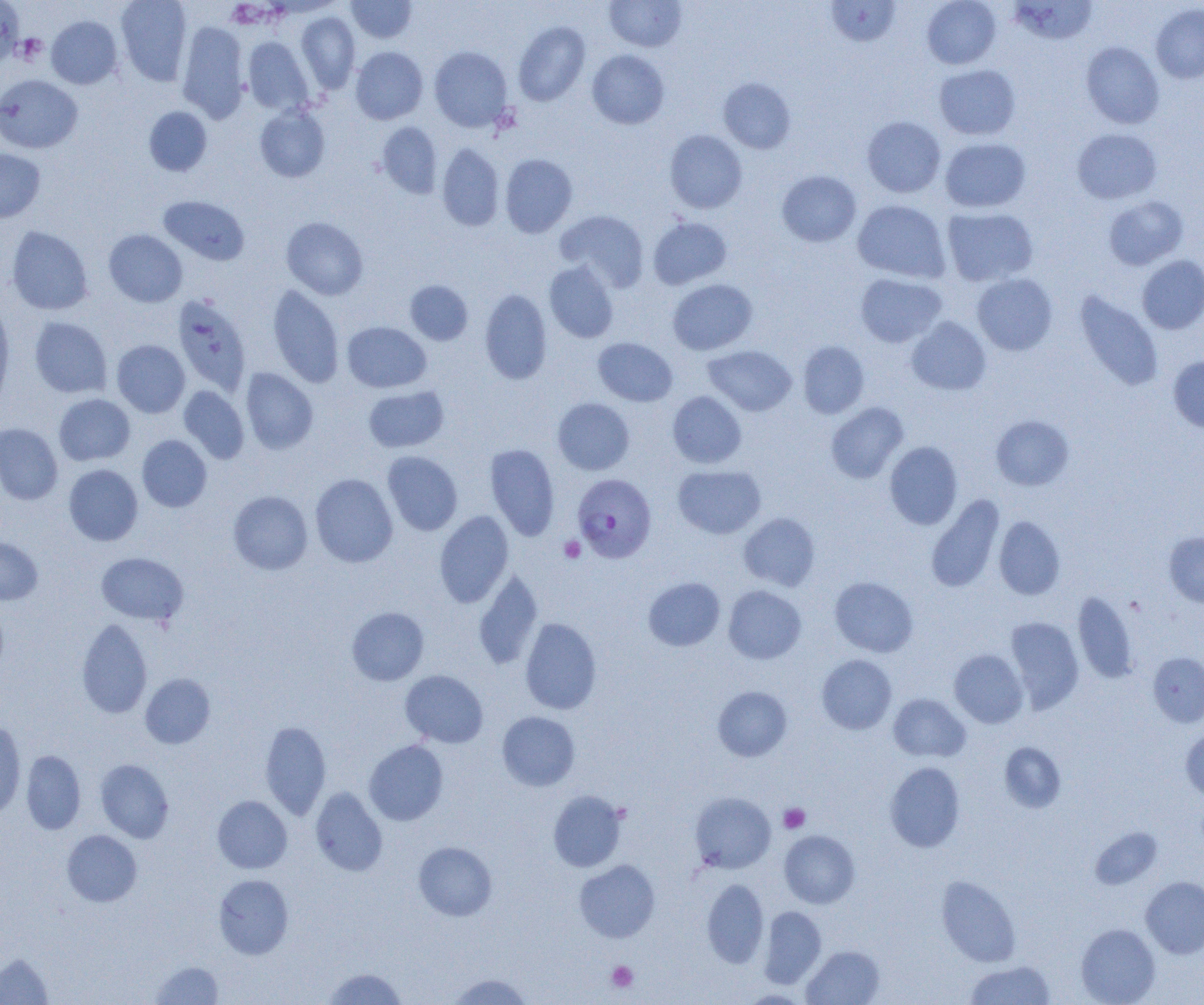
Approximate bounding boxes as [x1, y1, x2, y2] in pixels. Platelet locations: [16, 34, 47, 64], [558, 536, 585, 563], [779, 803, 810, 833], [606, 961, 638, 993]. Plasmodium falciparum-infected red blood cell locations: [573, 473, 656, 562]. Uninfected red blood cell locations: [115, 0, 192, 86], [346, 0, 418, 43], [605, 0, 687, 52], [825, 0, 901, 47], [922, 0, 1001, 69], [1010, 0, 1098, 45], [0, 1, 24, 68], [1150, 4, 1204, 84], [296, 11, 360, 94], [46, 15, 122, 89], [177, 21, 250, 122], [513, 21, 590, 106], [243, 36, 314, 115], [1081, 42, 1164, 129], [429, 46, 513, 131], [351, 47, 428, 125], [587, 50, 669, 129], [934, 64, 1021, 140], [0, 75, 82, 153], [718, 77, 796, 154], [255, 105, 330, 182], [144, 106, 212, 176], [862, 116, 946, 197], [377, 121, 443, 198], [1072, 128, 1161, 204], [664, 129, 748, 214], [940, 137, 1031, 212], [437, 143, 504, 231], [0, 148, 45, 222], [500, 154, 577, 238], [777, 170, 861, 247], [158, 195, 250, 266], [1103, 196, 1188, 270], [852, 200, 951, 282], [942, 207, 1038, 286], [555, 210, 649, 291], [281, 217, 369, 300], [648, 217, 732, 289], [6, 226, 93, 315], [104, 229, 187, 307], [1137, 255, 1204, 334], [544, 261, 618, 343], [855, 273, 947, 347], [972, 273, 1057, 355], [667, 279, 757, 355], [405, 280, 473, 346], [268, 284, 344, 388], [480, 288, 552, 385], [1074, 292, 1163, 391], [172, 294, 251, 395], [0, 297, 14, 410], [29, 317, 112, 398], [906, 317, 992, 395], [342, 321, 431, 393], [593, 337, 677, 406], [112, 340, 190, 417], [798, 341, 869, 418], [703, 345, 797, 416], [1168, 356, 1204, 432], [240, 368, 318, 454], [363, 385, 449, 453], [179, 386, 249, 463], [667, 391, 746, 468], [54, 394, 135, 465], [553, 398, 635, 475], [826, 402, 909, 483], [991, 415, 1074, 490], [0, 423, 63, 505], [137, 435, 212, 511], [884, 441, 963, 529], [484, 443, 560, 541], [382, 451, 462, 536], [63, 464, 143, 546], [673, 464, 766, 539], [310, 473, 398, 567], [228, 490, 313, 574], [926, 495, 1005, 592], [434, 511, 514, 607], [739, 513, 820, 590], [994, 516, 1065, 600], [1164, 531, 1204, 608], [0, 537, 43, 604], [96, 552, 188, 625], [472, 571, 544, 670], [643, 577, 725, 651], [830, 577, 918, 657], [723, 585, 806, 664], [1073, 591, 1137, 684], [347, 606, 429, 685], [520, 617, 602, 714], [1006, 617, 1084, 712], [77, 618, 153, 718], [949, 650, 1027, 728], [1148, 652, 1204, 727], [816, 654, 897, 734], [401, 669, 488, 747], [140, 673, 215, 749], [713, 686, 792, 761], [889, 694, 970, 762], [497, 711, 580, 791], [0, 719, 26, 821], [260, 720, 331, 819], [1181, 727, 1204, 800], [364, 740, 448, 825], [999, 741, 1066, 813], [21, 750, 86, 834], [96, 759, 174, 843], [885, 762, 965, 852], [310, 787, 388, 876], [548, 790, 627, 872], [690, 791, 776, 874], [212, 795, 292, 873], [1090, 827, 1162, 889], [62, 829, 142, 907], [779, 830, 860, 908], [413, 841, 497, 920], [574, 860, 660, 942], [214, 874, 294, 959], [936, 875, 1021, 966], [1140, 877, 1204, 958], [702, 878, 769, 968], [759, 905, 826, 988], [1076, 923, 1160, 1005], [802, 945, 884, 1005], [0, 953, 52, 1004], [150, 960, 224, 1004], [964, 960, 1056, 1005], [322, 967, 407, 1005], [446, 973, 534, 1004], [739, 989, 810, 1004]. Slide-level diagnosis: Plasmodium falciparum. Optical microscopy. Image is 1204×1005 pixels. Thin blood film. Single field of view. Captured at 1000x magnification.